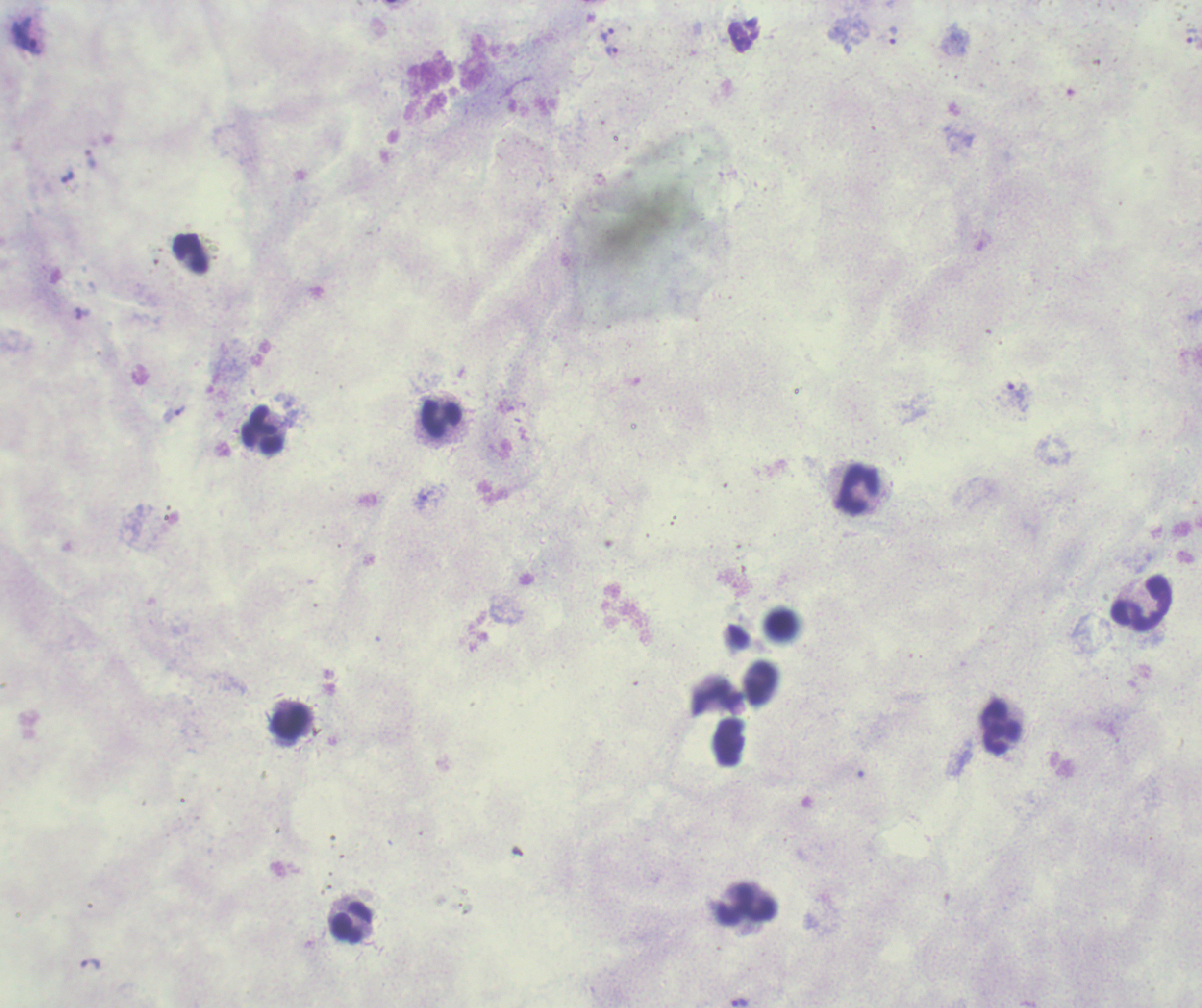

Approximate object centers, in pixels from the top-left corner. Leukocyte locations: (x=191, y=254), (x=440, y=417), (x=263, y=429), (x=857, y=487), (x=1142, y=603), (x=781, y=622), (x=760, y=681), (x=714, y=696), (x=290, y=721), (x=1002, y=727), (x=745, y=904), (x=352, y=923). Trophozoite locations: (x=607, y=35), (x=893, y=35), (x=27, y=37), (x=1192, y=38), (x=611, y=51), (x=90, y=159), (x=1016, y=393), (x=180, y=410), (x=421, y=500), (x=91, y=965), (x=740, y=1002). Previously used in an actual diagnosis. Background quality: unsatisfactory. Image is 1202×1008 pixels. Single field of view. Romanowsky-stained preparation. 100x magnification. Result: positive for malaria parasites. Thick blood film.